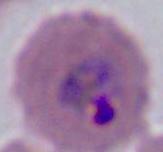

Summary:
  - Modality: micrograph
  - Identification: Plasmodium
  - Magnification: 400x or 1000x